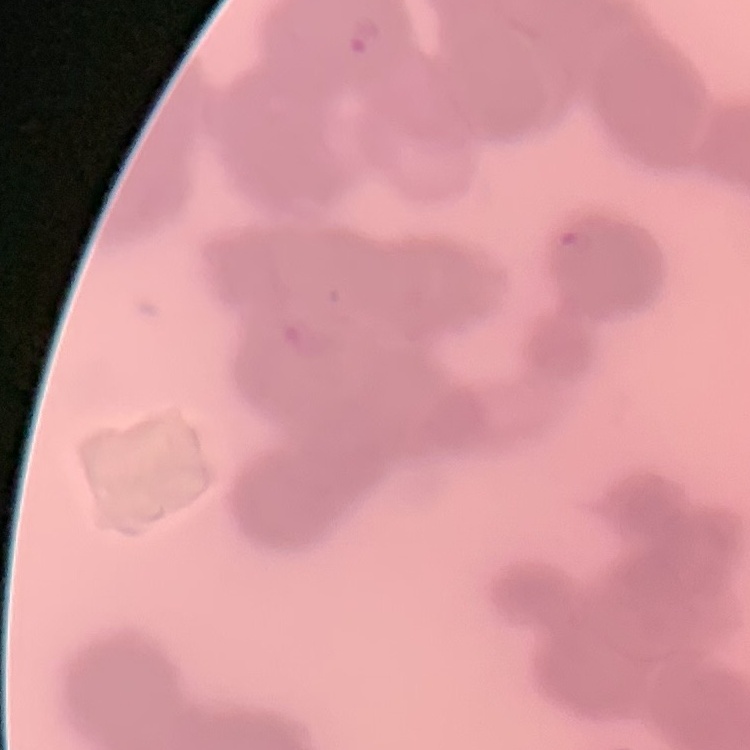 The red blood cells show rouleaux formation. Field's or Giemsa stain. Thin peripheral smear. Square crop of a larger photomicrograph.